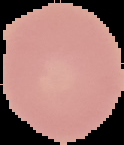
Cell region segmented out of the field of view; the surrounding area is masked to black. From a thin blood smear. Result: no malaria parasites seen. Image is 124×145 pixels.